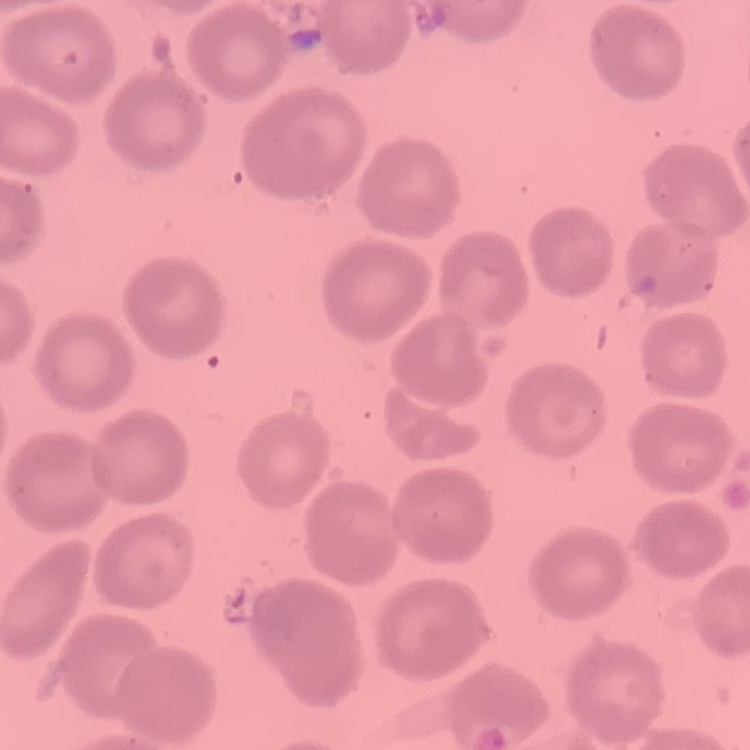
Summary:
  - Red blood cell morphology: no rouleaux formation
  - Image type: square crop of a larger photomicrograph
  - Stain: Field's or Giemsa
  - Preparation: thin blood film